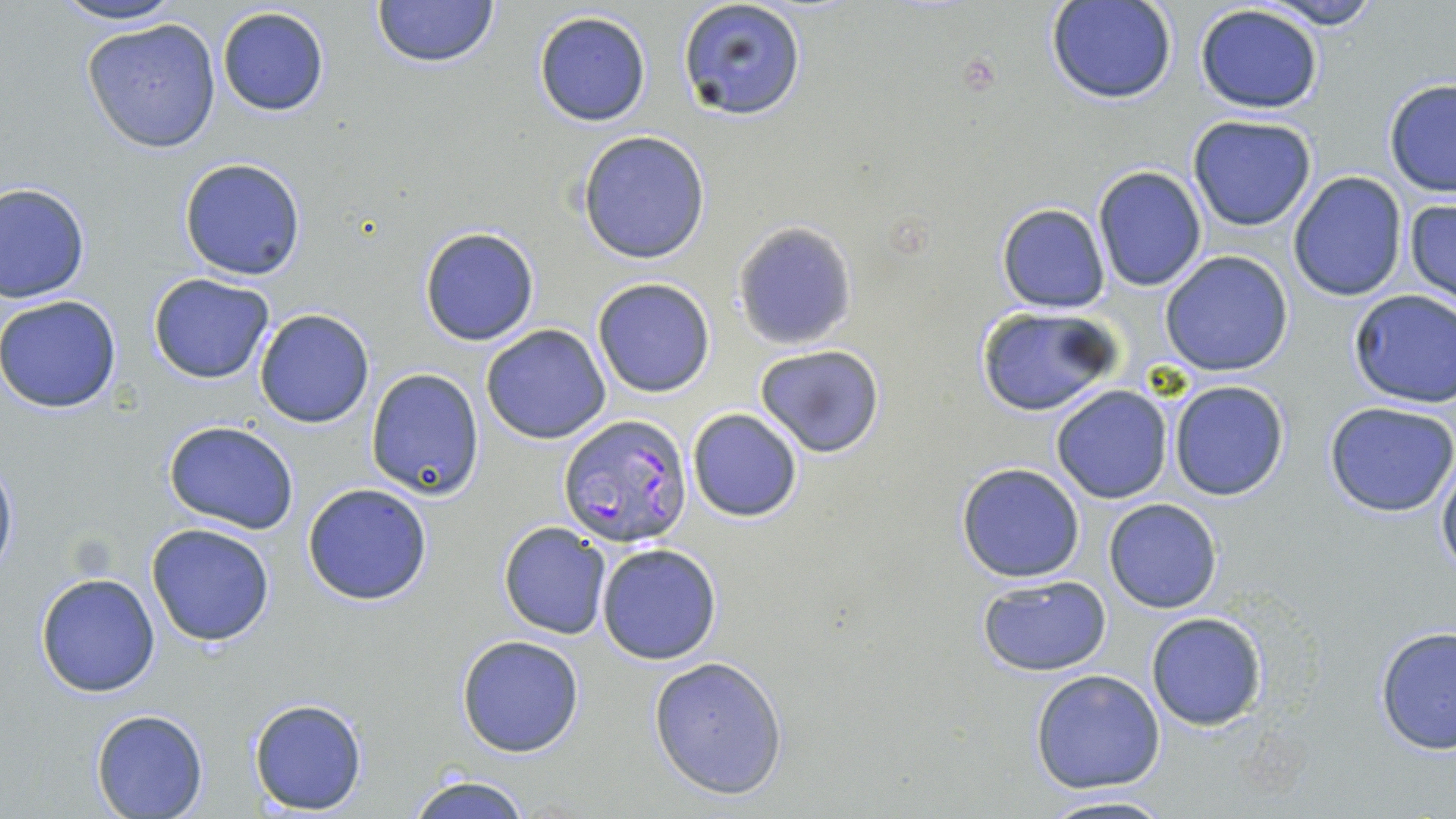

Summary:
  - Coordinate format: approximate bounding boxes as (x1,y1)-(x2,y2) corner pairs in pixels
  - Uninfected red blood cell locations: (48,0)-(187,28), (372,0)-(497,68), (1255,0)-(1385,30), (676,1)-(807,122), (1048,1)-(1177,105), (216,5)-(330,117), (1193,5)-(1324,113), (533,11)-(652,126), (80,18)-(223,153), (1383,79)-(1456,197), (1188,114)-(1317,231), (576,132)-(710,264), (178,157)-(306,281), (1092,165)-(1208,292), (1287,171)-(1406,302), (0,183)-(89,303), (1404,197)-(1455,307), (995,203)-(1110,313), (733,221)-(858,350), (419,227)-(540,346), (1159,252)-(1294,376), (148,273)-(275,383), (592,277)-(716,398), (1347,289)-(1456,409), (0,294)-(123,416), (974,305)-(1124,418), (253,310)-(375,428), (481,324)-(611,445), (754,344)-(886,459), (367,367)-(485,500), (1167,380)-(1290,501), (1050,386)-(1173,504), (1324,401)-(1456,516), (687,408)-(803,523), (163,421)-(299,534), (1437,450)-(1456,580), (0,454)-(18,583), (956,461)-(1087,583), (301,481)-(434,606), (1103,499)-(1222,614), (498,521)-(612,639), (146,522)-(276,647), (596,542)-(723,665), (35,571)-(162,697), (975,575)-(1113,674), (1145,611)-(1269,732), (1373,626)-(1456,755), (456,634)-(585,757), (648,656)-(788,799), (1030,668)-(1165,793), (248,697)-(368,815), (92,709)-(209,818), (405,772)-(534,819), (1033,792)-(1177,819)
  - Plasmodium falciparum-infected red blood cell locations: (556,412)-(694,547)
  - Slide-level diagnosis: Plasmodium falciparum
  - Field of view: one of a larger specimen
  - Preparation: thin blood smear
  - Stain: May-Grünwald-Giemsa
  - Modality: optical microscopy
  - Image size: 1456×819 pixels
  - Magnification: 1000x